Assess the morphology of the erythrocytes.
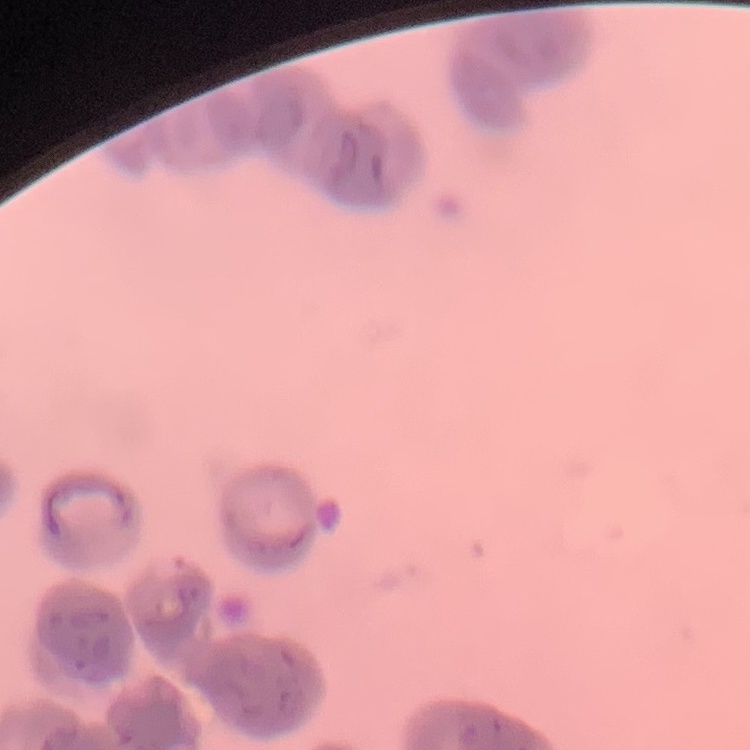

Rouleaux formation.

image type = one tile cut from a larger photomicrograph
stain = Field's or Giemsa
preparation = thin peripheral smear